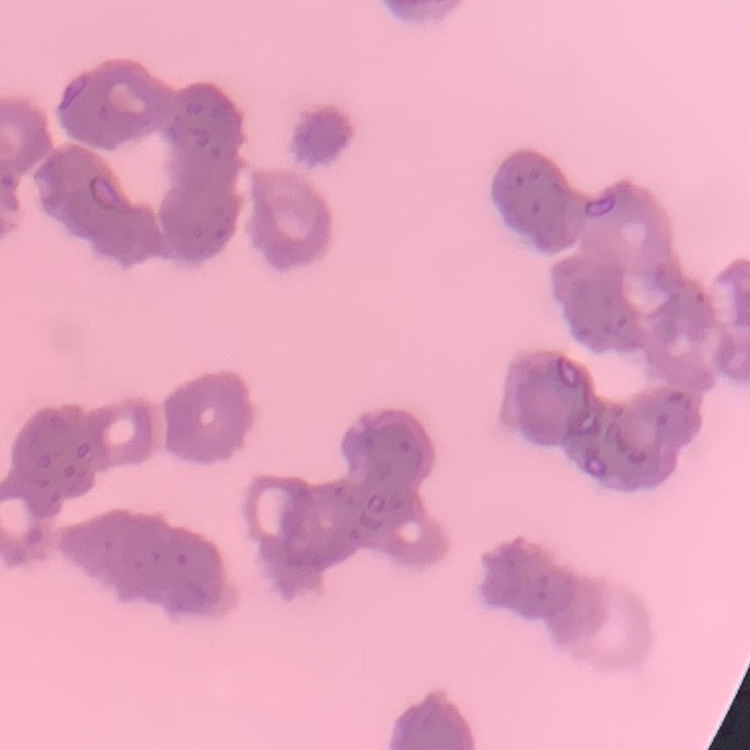

erythrocyte morphology = rouleaux formation
preparation = thin blood film
stain = Field's or Giemsa
image type = square crop of a larger photomicrograph